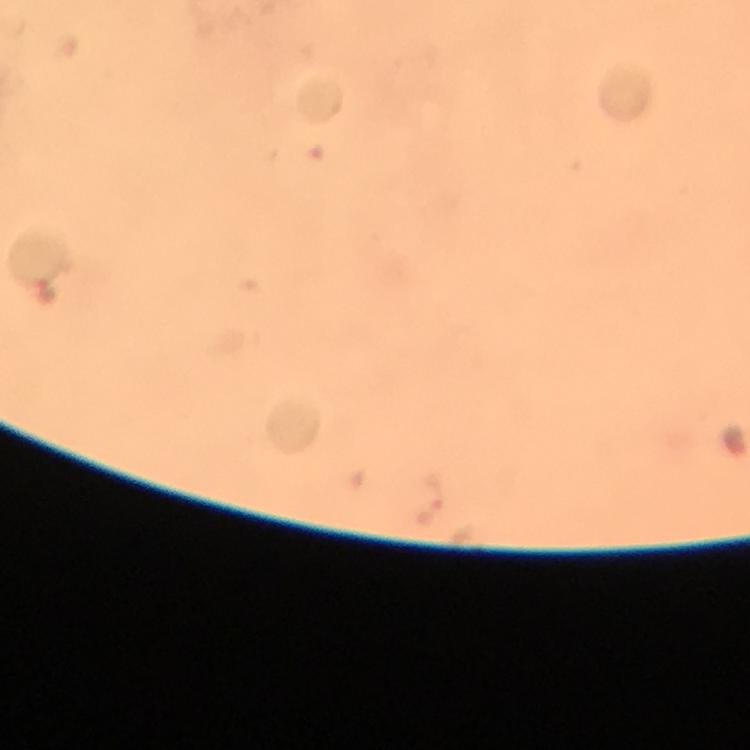

{
  "immersion_oil": "used",
  "stain": "Giemsa",
  "image_size": "750×750 pixels",
  "magnification": "100x",
  "plasmodium_parasite_locations": "approximate object centers, in pixels from the top-left corner: (x=45, y=292), (x=427, y=501)",
  "cropped_from": "one field of view",
  "context": "from a malaria diagnostic workup",
  "preparation": "thick blood smear",
  "capture": "smartphone photograph through a microscope"
}